Outline each Plasmodium ovale-infected red blood cell.
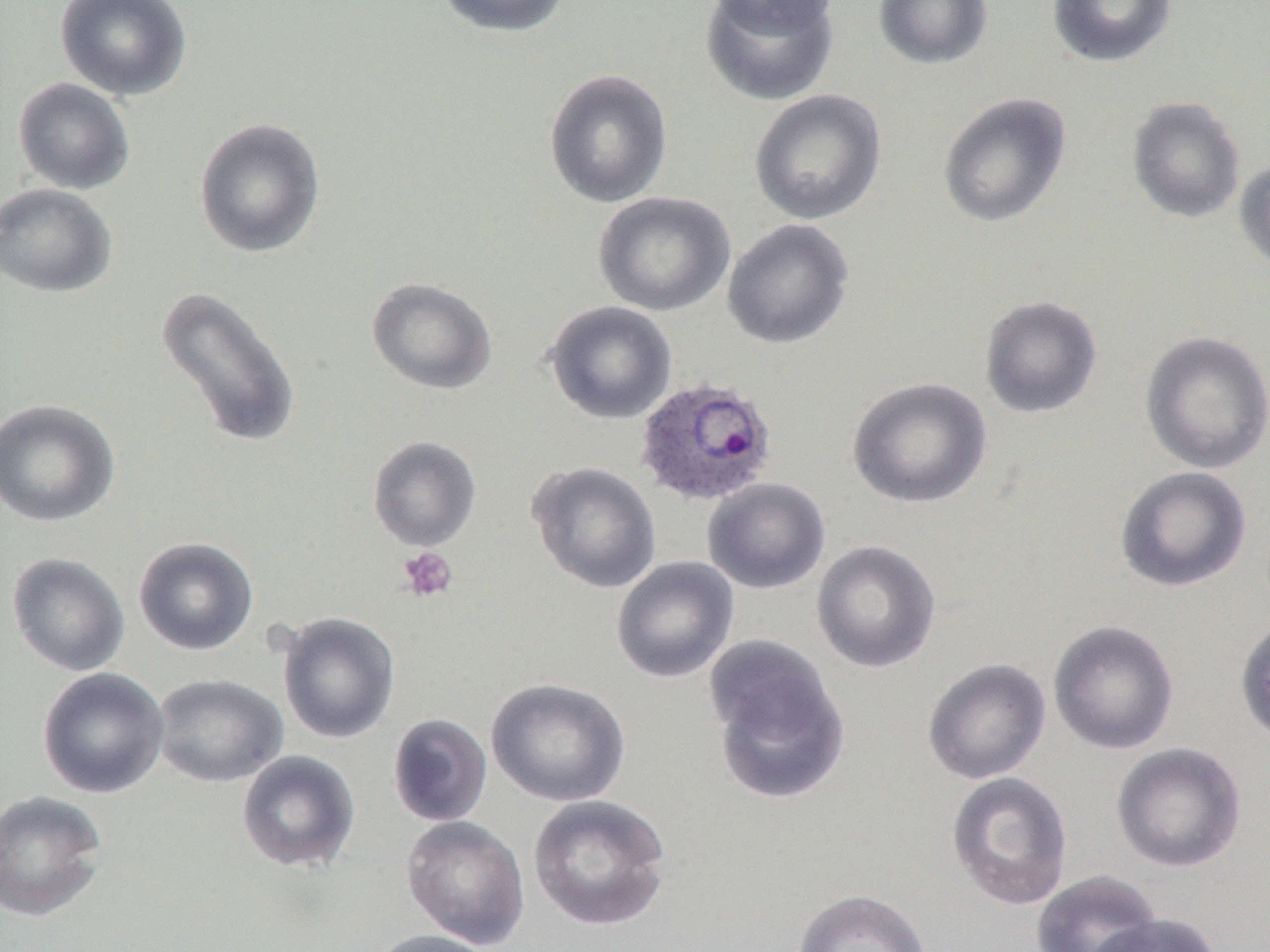
Approximate bounding boxes as (x1, y1, x2, y2) in pixels.
Plasmodium ovale-infected red blood cells: (634, 376, 778, 508).

Platelet locations: (398, 547, 458, 603). Uninfected red blood cell locations: (54, 0, 193, 102), (434, 0, 572, 38), (699, 0, 840, 106), (703, 0, 841, 33), (873, 0, 993, 70), (1046, 0, 1178, 68), (543, 68, 673, 208), (12, 77, 136, 195), (749, 88, 887, 225), (937, 92, 1072, 228), (1127, 96, 1246, 223), (194, 117, 326, 258), (1234, 158, 1270, 276), (0, 183, 118, 298), (593, 191, 736, 317), (722, 218, 854, 349), (366, 276, 498, 395), (155, 285, 302, 450), (979, 295, 1103, 419), (544, 300, 677, 425), (1139, 330, 1270, 474), (847, 376, 993, 509), (0, 398, 120, 527), (367, 435, 482, 552), (527, 461, 662, 593), (1115, 465, 1252, 593), (702, 477, 830, 594), (133, 536, 258, 656), (811, 540, 942, 673), (6, 552, 130, 677), (611, 556, 740, 683), (276, 611, 400, 744), (1234, 614, 1270, 748), (1048, 619, 1180, 755), (704, 635, 850, 804), (922, 657, 1051, 784), (37, 667, 169, 798), (153, 674, 288, 787), (486, 676, 631, 807), (388, 713, 493, 827), (1111, 741, 1247, 873), (237, 751, 361, 873), (947, 771, 1073, 911), (0, 789, 109, 922), (527, 794, 672, 931), (401, 815, 531, 949), (1031, 870, 1163, 952), (791, 888, 933, 952), (1087, 913, 1221, 952), (366, 929, 503, 952). Slide-level diagnosis: Plasmodium ovale. Light microscopy. One field of a larger specimen. Image is 1270×952 pixels. Captured at 1000x magnification. Thin blood smear.